Locate and identify every blood parasite.
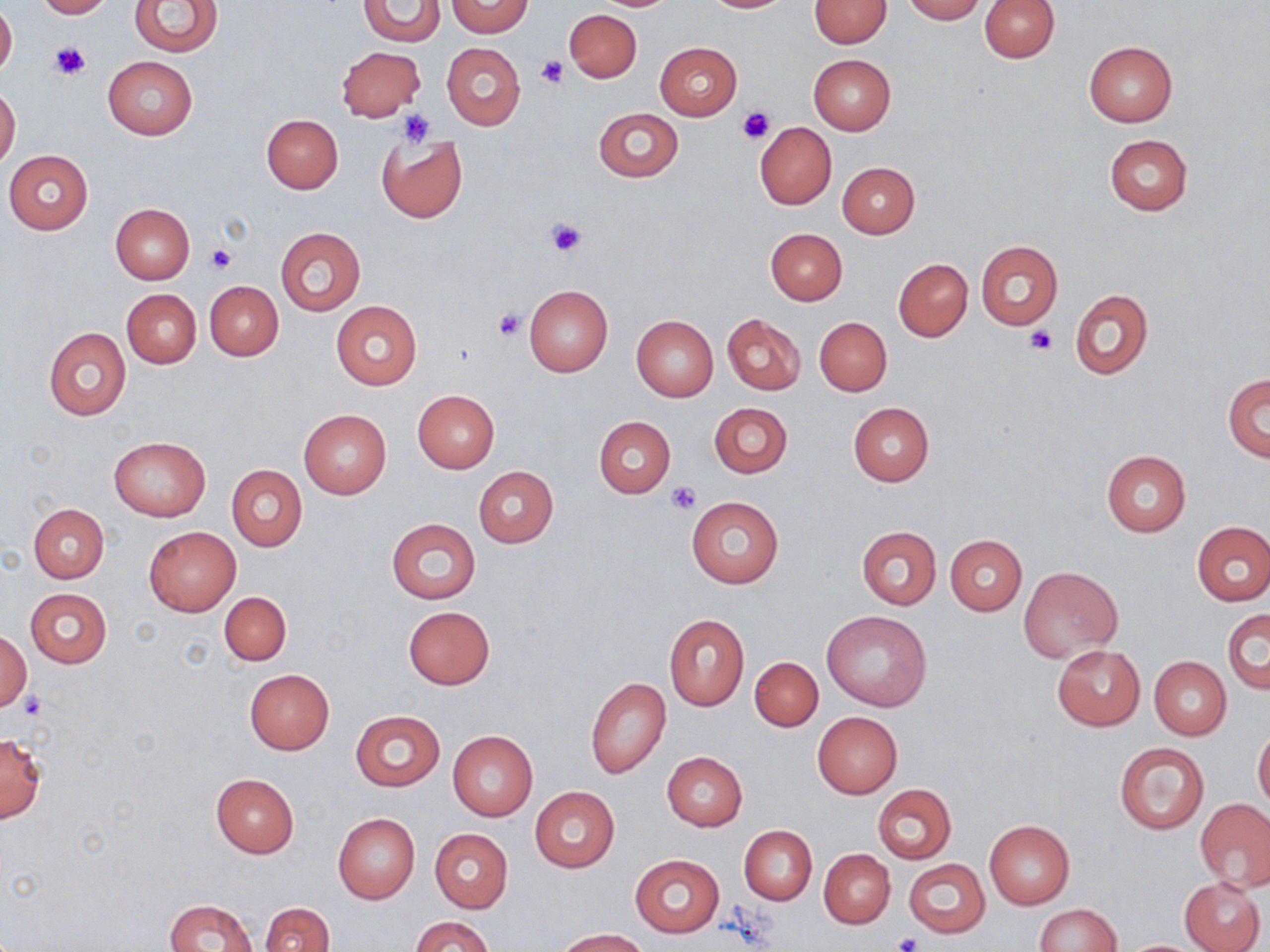
No blood parasites observed.

Summary:
  - Coordinate format: approximate bounding boxes as (x1,y1)-(x2,y2) corner pairs in pixels
  - Platelet locations: (49,42)-(89,78), (535,55)-(568,89), (739,106)-(774,142), (401,109)-(435,149), (546,216)-(589,260), (205,245)-(236,274), (493,308)-(527,342), (1027,326)-(1059,355), (667,481)-(702,514), (18,691)-(45,719), (890,931)-(923,952)
  - Uninfected red blood cell locations: (35,0)-(113,19), (703,0)-(789,13), (901,0)-(987,22), (979,0)-(1059,62), (131,1)-(223,56), (357,1)-(446,46), (447,1)-(531,37), (808,1)-(891,48), (0,5)-(17,79), (564,10)-(641,82), (1083,41)-(1176,127), (655,42)-(741,120), (442,43)-(525,130), (337,46)-(425,122), (808,53)-(896,134), (102,56)-(197,141), (0,85)-(20,169), (593,107)-(683,183), (261,115)-(343,194), (755,122)-(836,210), (377,133)-(468,223), (1104,134)-(1192,216), (4,149)-(93,233), (837,161)-(920,238), (110,203)-(194,284), (275,227)-(364,315), (765,228)-(848,305), (976,241)-(1063,329), (893,258)-(973,342), (204,281)-(283,360), (524,284)-(613,376), (122,289)-(201,368), (1070,289)-(1152,380), (330,300)-(423,390), (722,313)-(805,395), (631,314)-(718,401), (815,316)-(892,396), (43,327)-(131,421), (1224,373)-(1269,461), (412,390)-(500,473), (848,402)-(934,485), (709,403)-(792,477), (299,409)-(391,499), (594,416)-(676,498), (109,436)-(210,520), (1101,449)-(1190,536), (226,465)-(307,551), (473,466)-(558,547), (686,495)-(784,589), (28,503)-(108,582), (385,518)-(480,603), (1192,520)-(1269,605), (857,526)-(940,609), (143,527)-(240,617), (945,534)-(1026,615), (1017,565)-(1121,660), (24,588)-(112,668), (219,591)-(291,665), (403,606)-(494,689), (1223,609)-(1269,694), (822,611)-(932,712), (664,613)-(748,710), (1,632)-(31,712), (1052,645)-(1145,730), (1149,656)-(1231,739), (750,657)-(823,732), (245,669)-(334,753), (585,677)-(669,778), (350,710)-(445,791), (812,712)-(902,799), (1253,726)-(1270,809), (448,730)-(537,820), (0,735)-(46,823), (1114,741)-(1210,835), (662,751)-(746,831), (210,774)-(299,856), (873,783)-(956,864), (529,786)-(619,873), (1197,800)-(1270,891), (333,813)-(420,904), (984,820)-(1074,909), (739,825)-(816,905), (430,829)-(513,912), (820,848)-(894,927), (631,853)-(723,937), (904,858)-(989,937), (1179,876)-(1267,952), (164,899)-(259,951), (260,902)-(334,952), (1034,903)-(1121,952), (412,916)-(493,952), (554,929)-(647,951)
  - Slide-level diagnosis: negative for blood parasites
  - Preparation: thin blood smear
  - Stain: May-Grünwald-Giemsa
  - Field of view: single
  - Image size: 1270×952 pixels
  - Modality: light microscopy
  - Magnification: 1000x